Name the blood parasite species.
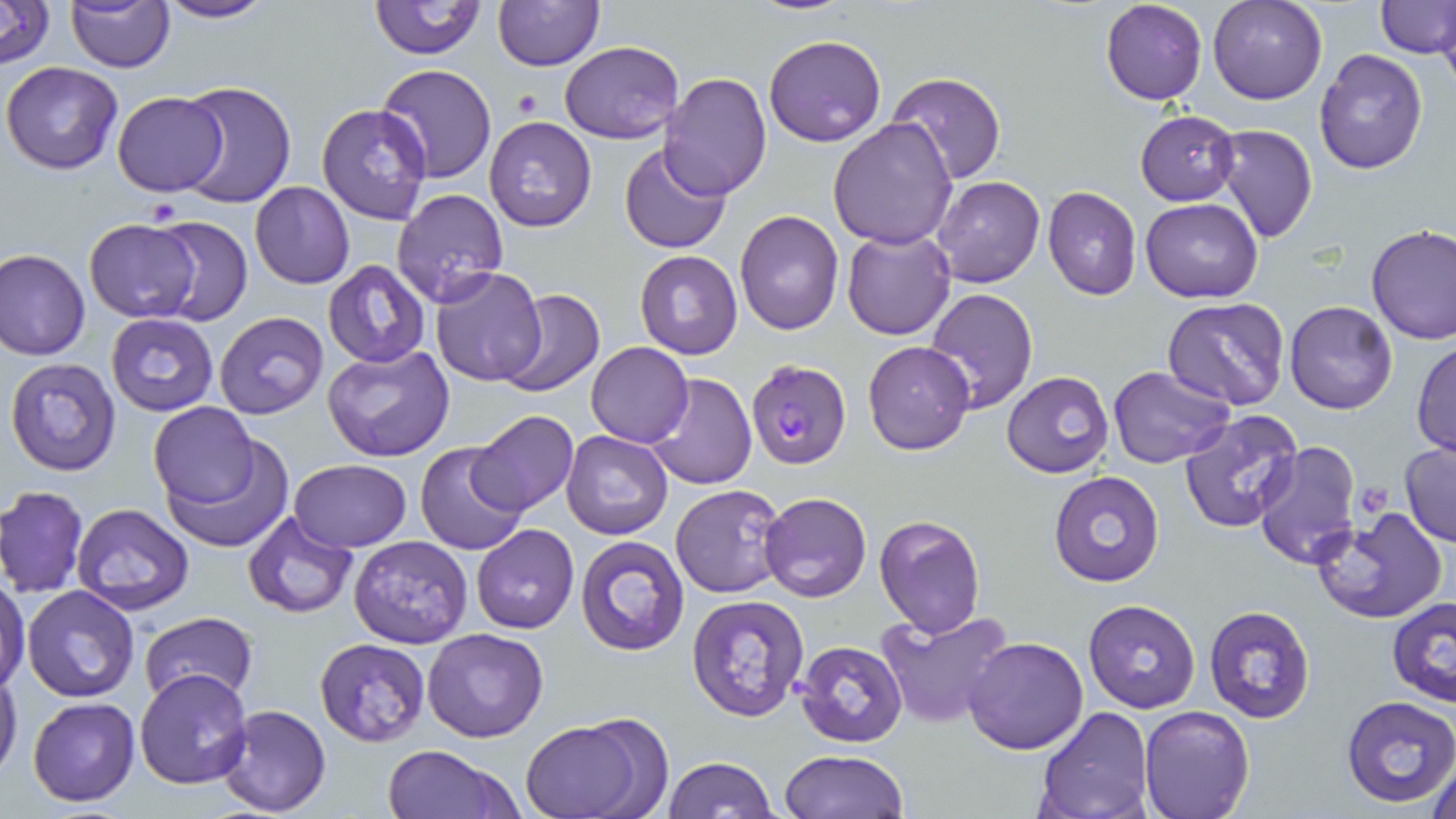

Plasmodium falciparum.

stain = May-Grünwald-Giemsa
uninfected red blood cell locations = approximate bounding boxes as (x1, y1, x2, y2) in pixels: (0, 0, 56, 69), (152, 0, 277, 24), (371, 0, 485, 60), (1100, 0, 1207, 105), (1208, 0, 1327, 105), (1377, 0, 1456, 58), (493, 1, 603, 70), (67, 2, 173, 72), (1439, 12, 1456, 98), (765, 34, 886, 147), (559, 40, 684, 144), (1314, 49, 1428, 175), (1, 61, 124, 174), (377, 63, 495, 183), (885, 71, 1004, 186), (659, 72, 772, 199), (173, 79, 295, 209), (111, 91, 227, 196), (317, 103, 432, 224), (1135, 111, 1239, 204), (483, 116, 598, 233), (829, 116, 958, 249), (1212, 123, 1317, 243), (619, 142, 733, 253), (933, 177, 1045, 288), (250, 181, 353, 290), (1042, 185, 1142, 300), (390, 189, 508, 309), (1141, 198, 1264, 302), (734, 209, 843, 335), (145, 215, 254, 325), (83, 217, 202, 323), (1366, 224, 1456, 347), (842, 227, 957, 341), (1, 248, 90, 362), (636, 250, 742, 359), (322, 259, 430, 368), (430, 266, 546, 386), (924, 287, 1039, 414), (494, 289, 604, 398), (1163, 296, 1291, 411), (1284, 300, 1399, 415), (215, 311, 327, 419), (106, 312, 219, 417), (863, 339, 976, 455), (587, 341, 692, 447), (1411, 341, 1456, 455), (323, 344, 456, 463), (5, 356, 123, 477), (1106, 364, 1234, 469), (1002, 370, 1114, 477), (644, 373, 756, 490), (150, 401, 261, 509), (466, 410, 578, 516), (1181, 410, 1306, 533), (561, 430, 672, 540), (161, 432, 294, 552), (1252, 440, 1362, 570), (415, 441, 529, 557), (1398, 441, 1456, 548), (288, 459, 413, 552), (1047, 470, 1163, 587), (670, 484, 789, 598), (1, 486, 88, 596), (759, 492, 871, 604), (71, 502, 195, 613), (1312, 507, 1448, 625), (242, 511, 359, 619), (874, 515, 986, 638), (471, 524, 578, 633), (347, 535, 473, 647), (574, 536, 691, 656), (0, 576, 28, 694), (22, 585, 138, 701), (687, 592, 812, 721), (1387, 598, 1456, 707), (1083, 599, 1200, 713), (1204, 606, 1315, 723), (875, 609, 1011, 730), (137, 611, 259, 708), (422, 628, 549, 743), (964, 636, 1089, 754), (314, 637, 431, 746), (794, 640, 907, 748), (0, 666, 22, 781), (133, 670, 252, 790), (1339, 695, 1456, 809), (27, 697, 141, 806), (216, 704, 332, 817), (1034, 706, 1153, 819), (1138, 706, 1255, 819), (519, 718, 652, 819), (383, 745, 514, 819), (778, 750, 909, 818), (1424, 755, 1456, 819), (662, 757, 779, 817)
magnification = 1000x
modality = light microscopy
field of view = one of a larger specimen
preparation = thin blood smear
image size = 1456×819 pixels
Plasmodium falciparum-infected red blood cell locations = approximate bounding boxes as (x1, y1, x2, y2) in pixels: (745, 358, 851, 469)
platelet locations = approximate bounding boxes as (x1, y1, x2, y2) in pixels: (513, 89, 543, 117)